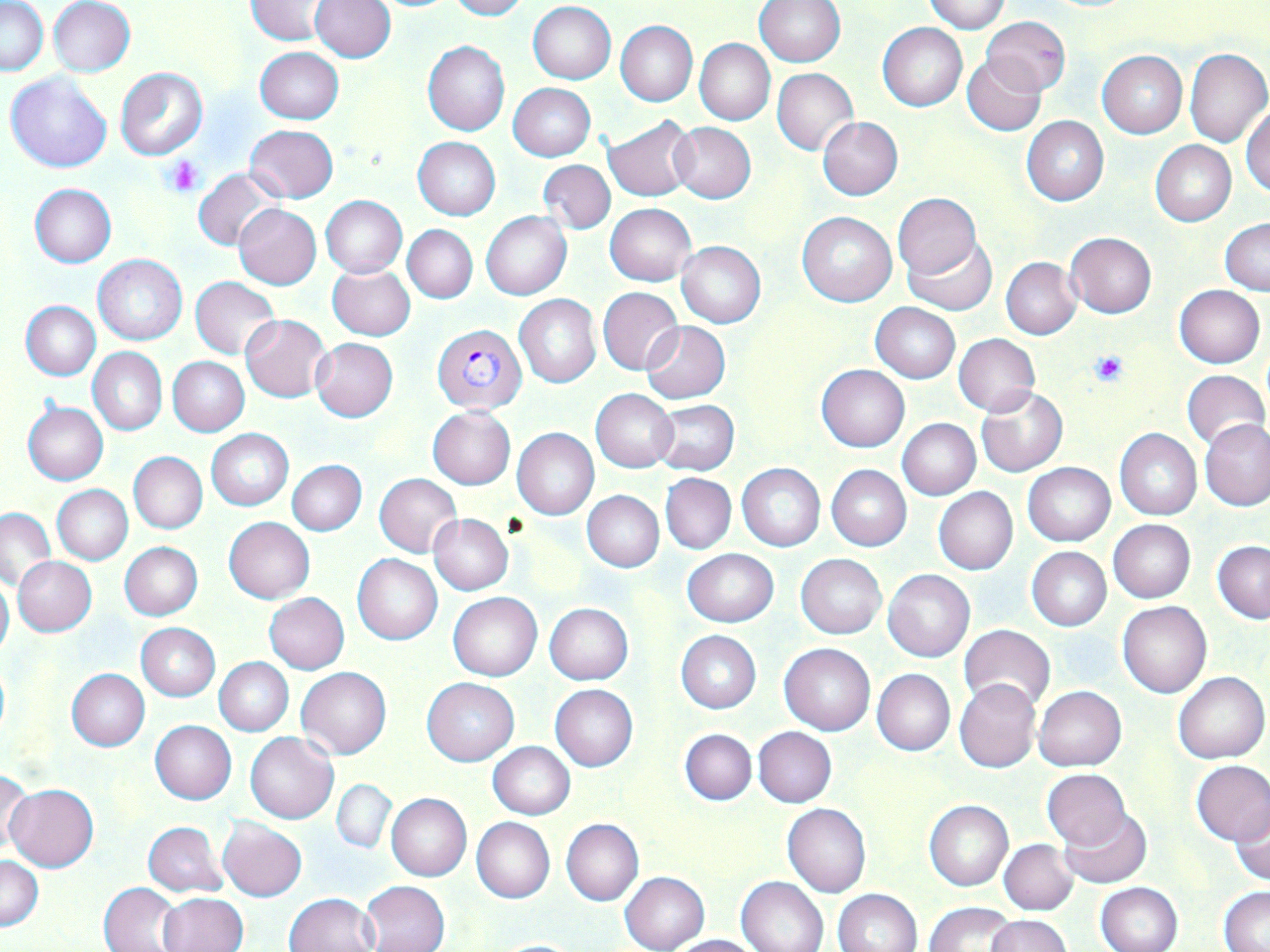
Summary:
  - Coordinate format: approximate bounding boxes as [x1, y1, x2, y2] in pixels
  - Plasmodium falciparum-infected red blood cell locations: [432, 325, 526, 414]
  - Uninfected red blood cell locations: [1, 0, 47, 75], [48, 0, 135, 77], [245, 0, 334, 44], [310, 0, 395, 62], [445, 0, 528, 20], [924, 0, 1010, 34], [755, 1, 844, 68], [528, 2, 616, 84], [980, 15, 1071, 94], [615, 19, 698, 106], [878, 21, 967, 111], [695, 39, 775, 125], [422, 41, 510, 136], [255, 47, 343, 124], [1184, 48, 1270, 147], [1098, 51, 1188, 135], [963, 55, 1046, 135], [115, 68, 207, 159], [772, 68, 858, 154], [4, 72, 112, 173], [508, 84, 595, 161], [1242, 104, 1270, 197], [603, 116, 698, 201], [1022, 116, 1109, 206], [819, 117, 902, 200], [669, 122, 756, 204], [244, 124, 338, 202], [413, 137, 500, 220], [1151, 140, 1236, 226], [537, 159, 615, 234], [195, 169, 282, 251], [29, 183, 116, 267], [893, 194, 982, 276], [321, 195, 407, 277], [605, 203, 697, 286], [233, 204, 322, 289], [481, 211, 571, 300], [797, 211, 896, 307], [1220, 218, 1270, 294], [403, 225, 477, 303], [1065, 232, 1157, 318], [902, 235, 996, 314], [675, 240, 765, 328], [93, 254, 187, 345], [1002, 257, 1081, 339], [327, 263, 415, 341], [191, 276, 279, 359], [1173, 284, 1265, 368], [597, 287, 683, 375], [514, 294, 601, 388], [20, 301, 101, 381], [870, 303, 960, 383], [241, 314, 333, 403], [641, 321, 730, 403], [953, 334, 1040, 417], [311, 338, 398, 422], [88, 347, 167, 435], [168, 356, 250, 437], [816, 364, 909, 451], [1181, 370, 1268, 451], [975, 385, 1068, 477], [591, 389, 677, 473], [651, 400, 739, 477], [24, 402, 108, 484], [427, 407, 515, 489], [898, 418, 981, 500], [1202, 418, 1269, 511], [512, 428, 599, 520], [206, 429, 294, 511], [1114, 429, 1202, 520], [129, 451, 208, 534], [288, 459, 366, 536], [1022, 462, 1115, 545], [737, 464, 825, 550], [826, 465, 911, 549], [374, 473, 461, 556], [661, 473, 736, 554], [52, 485, 132, 565], [933, 488, 1017, 574], [581, 490, 663, 572], [1, 507, 54, 590], [429, 513, 513, 595], [224, 517, 315, 603], [1109, 520, 1195, 603], [1212, 541, 1270, 623], [120, 542, 203, 620], [1025, 547, 1111, 632], [683, 548, 778, 627], [352, 553, 442, 644], [796, 554, 887, 639], [14, 556, 96, 636], [883, 569, 975, 662], [0, 572, 13, 664], [449, 592, 542, 680], [265, 593, 349, 674], [1117, 600, 1211, 699], [545, 603, 634, 685], [137, 624, 220, 700], [959, 625, 1056, 712], [676, 630, 761, 712], [779, 644, 874, 734], [214, 657, 293, 736], [297, 666, 391, 759], [65, 669, 149, 751], [871, 669, 955, 756], [1172, 671, 1269, 763], [421, 677, 519, 765], [954, 679, 1039, 772], [550, 684, 637, 771], [1035, 686, 1127, 770], [150, 720, 236, 805], [754, 726, 837, 807], [679, 728, 757, 805], [244, 732, 337, 824], [487, 742, 575, 819], [1190, 760, 1270, 844], [1042, 769, 1131, 849], [0, 770, 32, 857], [333, 779, 398, 852], [6, 783, 98, 872], [386, 793, 472, 881], [924, 800, 1014, 890], [1230, 803, 1270, 886], [783, 804, 871, 897], [1059, 809, 1152, 889], [219, 818, 307, 901], [471, 818, 554, 903], [561, 818, 643, 906], [144, 821, 228, 897], [998, 839, 1078, 914], [0, 856, 42, 930], [620, 872, 710, 951], [737, 875, 829, 952], [99, 881, 183, 952], [360, 881, 450, 952], [1094, 882, 1182, 952], [1219, 886, 1270, 950], [832, 889, 921, 952], [159, 892, 248, 952], [285, 892, 380, 952], [925, 901, 1019, 952], [986, 914, 1070, 952], [672, 934, 763, 952], [485, 938, 588, 951]
  - Platelet locations: [166, 156, 204, 195], [1089, 349, 1129, 387]
  - Slide-level diagnosis: Plasmodium falciparum
  - Stain: May-Grünwald-Giemsa
  - Modality: light microscopy
  - Image size: 1270×952 pixels
  - Field of view: single
  - Preparation: thin blood film
  - Magnification: 1000x